Point out leukocytes.
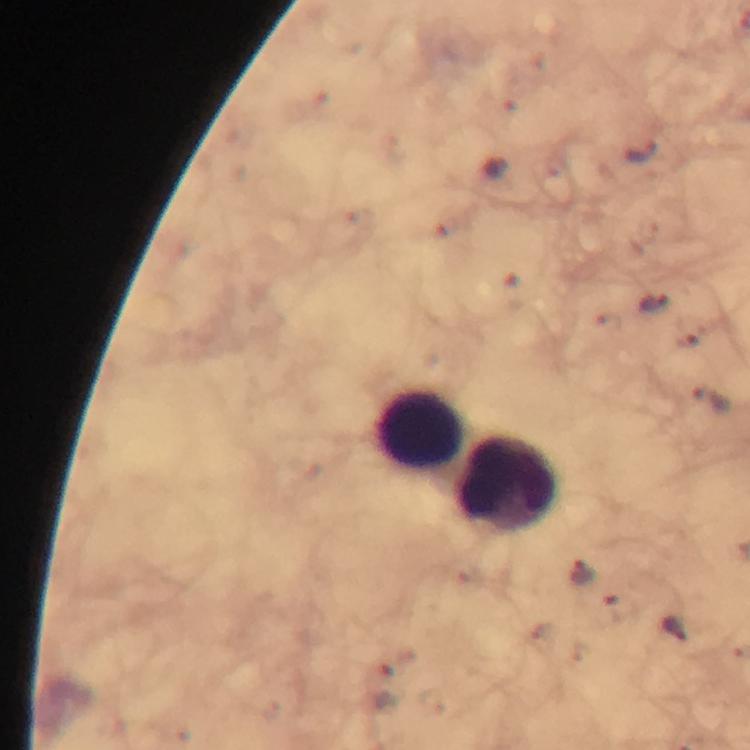
Approximate centers as (x, y) in pixels.
Leukocytes: (418, 428), (508, 484).

stain = Giemsa
image size = 750×750 pixels
malaria parasite locations = approximate centers as (x, y) in pixels: (645, 152), (496, 168), (655, 300), (708, 399), (582, 573), (674, 627)
immersion oil = used
context = from a malaria diagnostic workup
cropped from = a single field of view
capture = smartphone photograph through a microscope
magnification = 100x
preparation = thick blood film